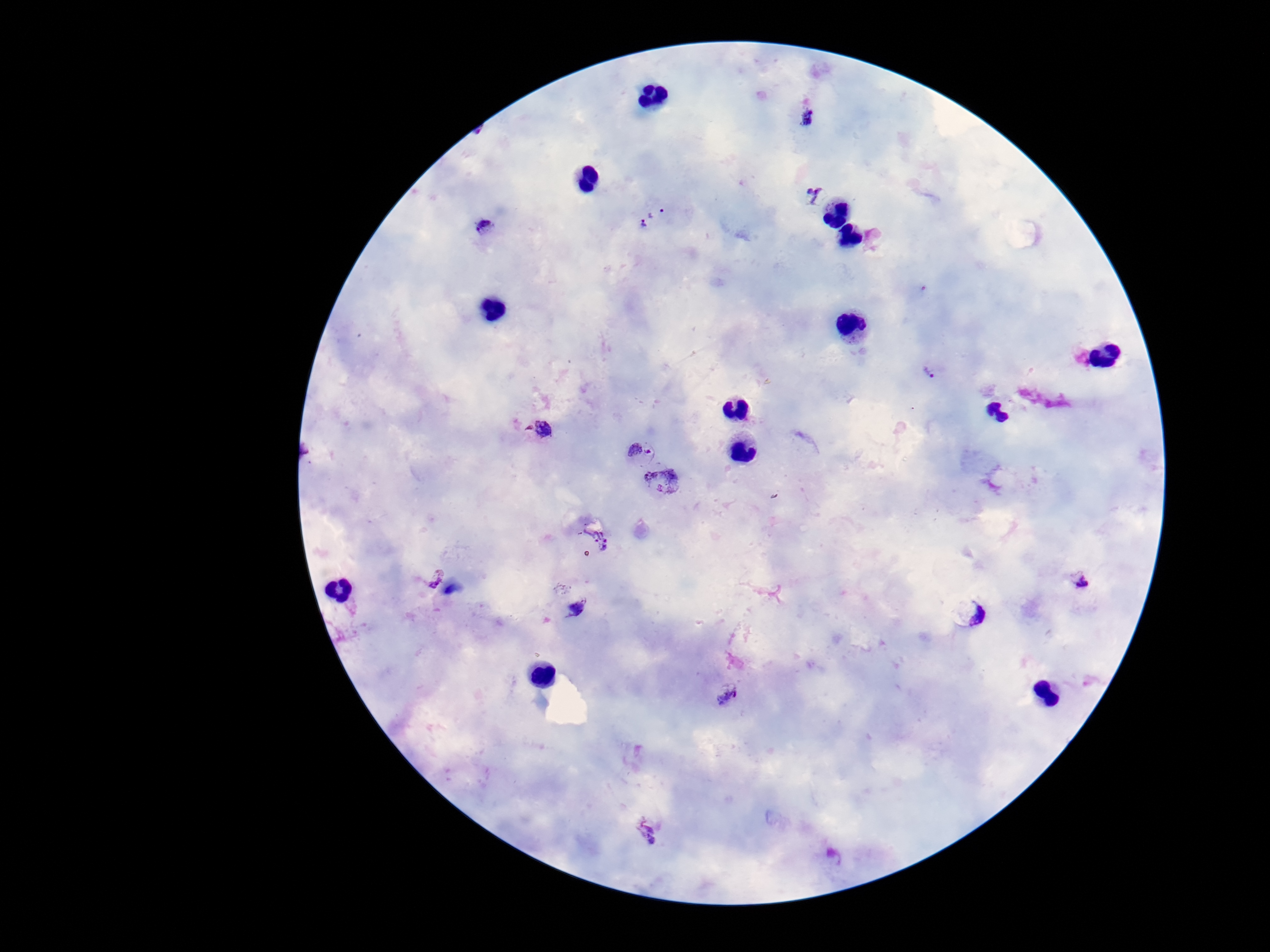 Approximate object centers, in pixels from the top-left corner. Plasmodium parasite locations: (x=808, y=117), (x=816, y=196), (x=657, y=212), (x=484, y=227), (x=643, y=227), (x=930, y=372), (x=544, y=429), (x=639, y=451), (x=664, y=484), (x=595, y=537), (x=436, y=578), (x=1080, y=582), (x=573, y=609), (x=969, y=612), (x=726, y=694), (x=645, y=831). Giemsa-stained preparation. One field from this slide. Image is 1270×952 pixels. Patient malaria status: infected. 100x magnification. Photographed through the microscope eyepiece with a smartphone camera. Thick blood film.